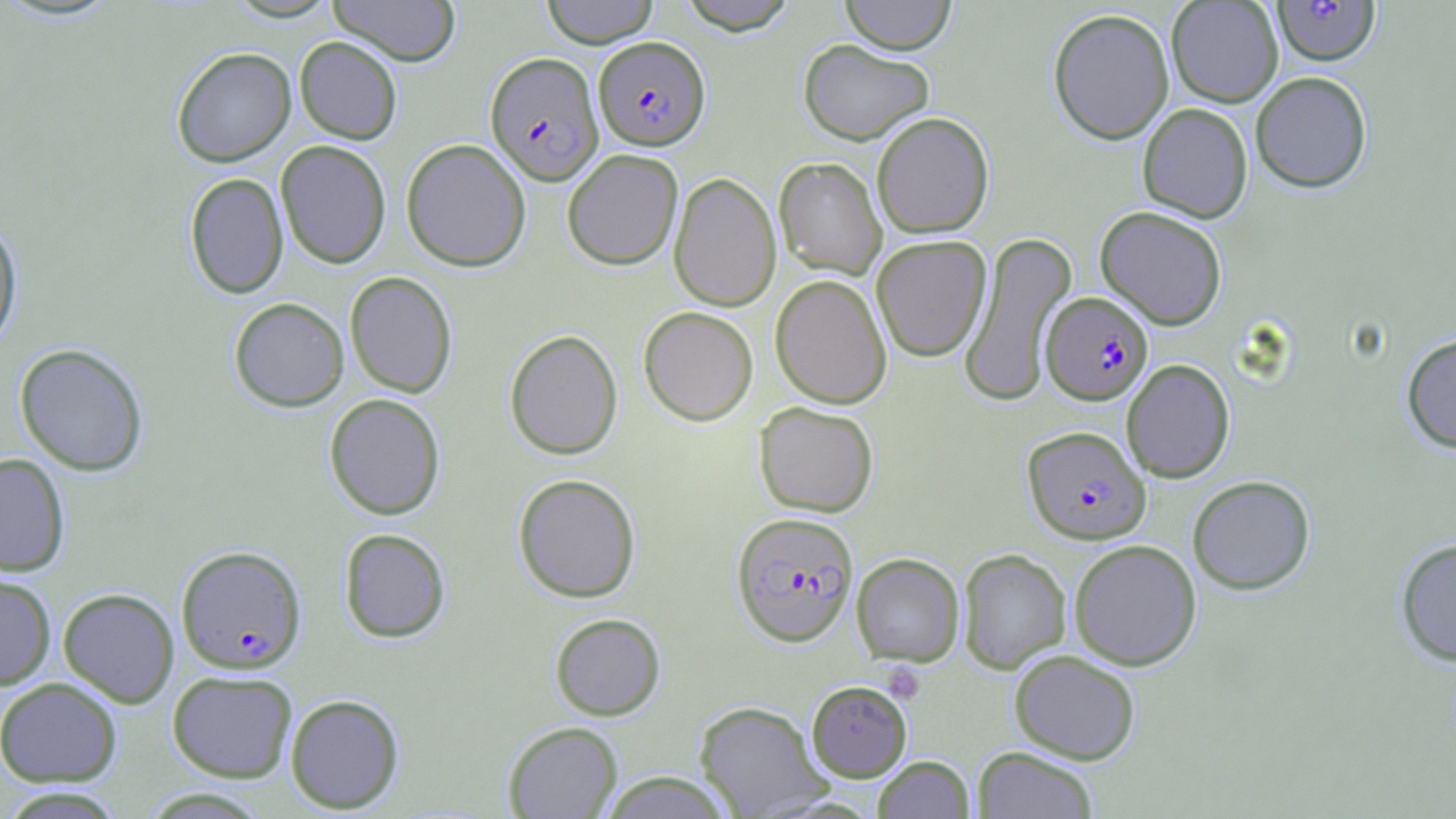

Summary:
  - Coordinate format: approximate bounding boxes as (x1,y1)-(x2,y2) corner pairs in pixels
  - Uninfected red blood cell locations: (328,0)-(462,66), (541,0)-(659,47), (677,0)-(799,34), (839,0)-(957,54), (1166,0)-(1283,107), (1048,8)-(1174,145), (295,37)-(402,144), (798,39)-(934,145), (172,47)-(296,166), (1250,71)-(1372,193), (1137,103)-(1253,223), (872,112)-(994,239), (401,138)-(531,271), (275,140)-(391,269), (562,149)-(683,270), (774,157)-(887,280), (185,172)-(289,299), (669,172)-(781,311), (1095,206)-(1228,329), (0,216)-(23,353), (959,230)-(1078,406), (871,235)-(991,362), (345,271)-(457,398), (770,274)-(892,409), (229,297)-(349,412), (638,306)-(759,425), (504,329)-(623,460), (1401,333)-(1456,453), (14,343)-(149,476), (1121,359)-(1235,483), (324,393)-(446,520), (754,401)-(879,517), (0,452)-(70,576), (513,473)-(641,603), (1188,475)-(1315,595), (338,528)-(451,643), (1395,538)-(1456,666), (1068,539)-(1202,670), (957,548)-(1071,674), (851,553)-(964,667), (0,572)-(56,690), (58,588)-(179,707), (549,613)-(666,720), (1009,649)-(1141,764), (167,670)-(298,783), (0,676)-(122,787), (806,680)-(912,782), (285,693)-(404,814), (694,700)-(832,818), (502,721)-(623,818), (972,746)-(1099,818), (873,756)-(975,818), (599,771)-(736,818), (1,788)-(128,818)
  - Plasmodium falciparum-infected red blood cell locations: (1272,1)-(1381,66), (593,36)-(710,150), (484,52)-(604,185), (1041,291)-(1153,405), (1023,425)-(1150,544), (731,511)-(859,646), (176,544)-(307,674)
  - Platelet locations: (882,663)-(925,703)
  - Slide-level diagnosis: Plasmodium falciparum
  - Stain: May-Grünwald-Giemsa
  - Image size: 1456×819 pixels
  - Field of view: one of a larger specimen
  - Preparation: thin blood smear
  - Magnification: 1000x
  - Modality: light microscopy